Identify the blood parasite species.
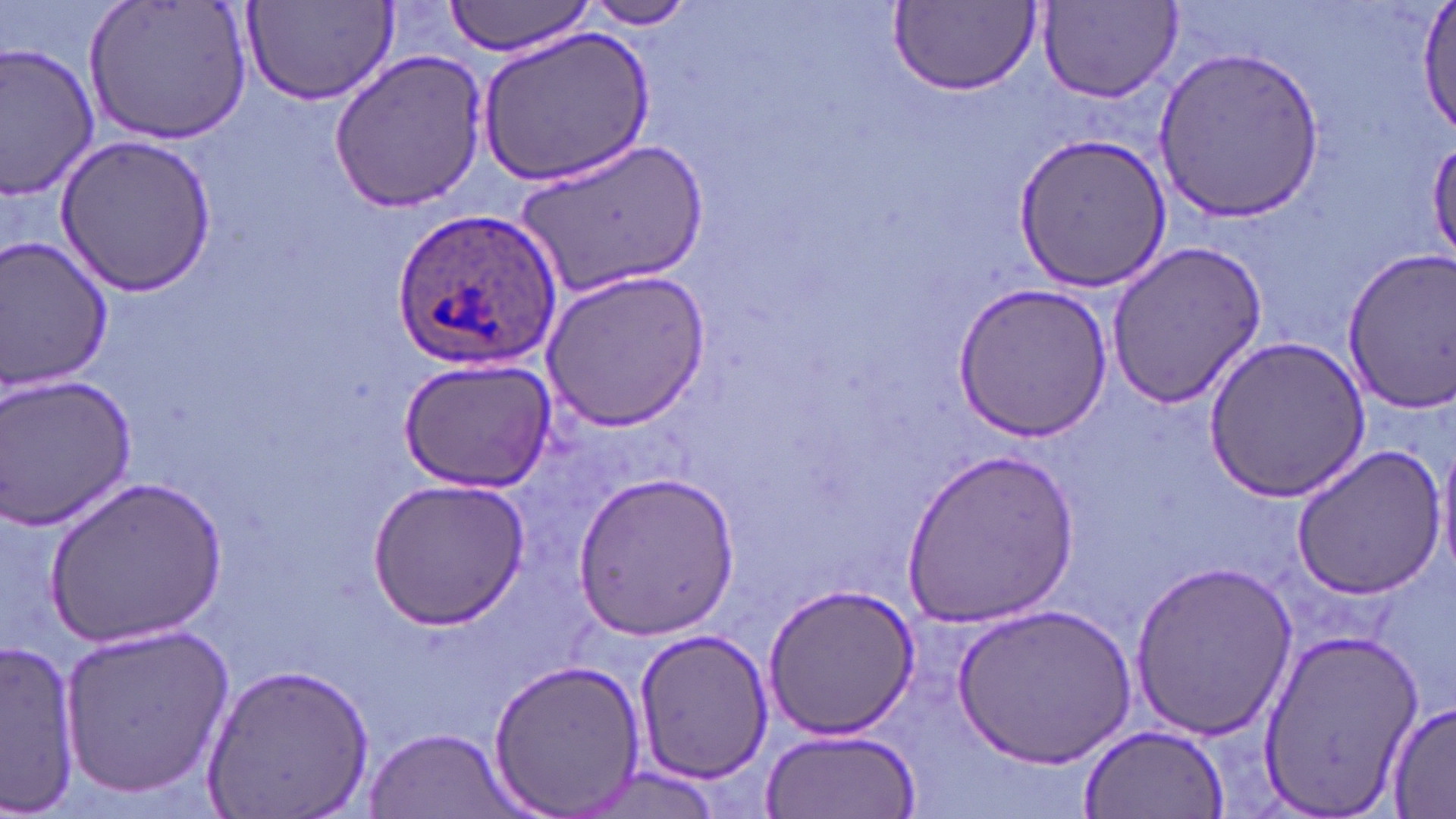
Plasmodium ovale.

Approximate bounding boxes as named x1/y1/x2/y2 corners in pixels. Plasmodium ovale-infected red blood cell locations: (x1=394, y1=206, x2=564, y2=369). Uninfected red blood cell locations: (x1=85, y1=0, x2=253, y2=144), (x1=440, y1=0, x2=600, y2=55), (x1=1414, y1=0, x2=1456, y2=137), (x1=581, y1=1, x2=698, y2=29), (x1=890, y1=2, x2=1041, y2=95), (x1=1036, y1=2, x2=1183, y2=104), (x1=242, y1=3, x2=397, y2=107), (x1=479, y1=28, x2=654, y2=185), (x1=0, y1=41, x2=100, y2=202), (x1=1155, y1=44, x2=1323, y2=225), (x1=326, y1=49, x2=492, y2=211), (x1=1012, y1=131, x2=1172, y2=295), (x1=54, y1=135, x2=221, y2=298), (x1=515, y1=136, x2=706, y2=301), (x1=1428, y1=137, x2=1456, y2=269), (x1=0, y1=236, x2=115, y2=397), (x1=1106, y1=239, x2=1269, y2=411), (x1=1340, y1=252, x2=1455, y2=411), (x1=539, y1=268, x2=711, y2=430), (x1=954, y1=283, x2=1112, y2=442), (x1=1203, y1=336, x2=1370, y2=501), (x1=397, y1=355, x2=556, y2=493), (x1=0, y1=374, x2=139, y2=531), (x1=1436, y1=435, x2=1456, y2=583), (x1=1289, y1=444, x2=1448, y2=601), (x1=897, y1=448, x2=1081, y2=627), (x1=575, y1=469, x2=739, y2=638), (x1=47, y1=477, x2=228, y2=646), (x1=368, y1=477, x2=529, y2=627), (x1=1127, y1=559, x2=1297, y2=740), (x1=764, y1=582, x2=920, y2=739), (x1=954, y1=605, x2=1133, y2=769), (x1=58, y1=620, x2=234, y2=800), (x1=1256, y1=627, x2=1421, y2=819), (x1=632, y1=628, x2=772, y2=785), (x1=1, y1=639, x2=81, y2=812), (x1=486, y1=656, x2=647, y2=816), (x1=202, y1=661, x2=374, y2=818), (x1=1386, y1=699, x2=1456, y2=816), (x1=1076, y1=722, x2=1230, y2=818), (x1=760, y1=727, x2=921, y2=816), (x1=364, y1=729, x2=518, y2=818), (x1=572, y1=768, x2=726, y2=817). 1000x magnification. Thin blood film. Single field of view. Image is 1456×819 pixels. Optical microscopy. May-Grünwald-Giemsa stain.